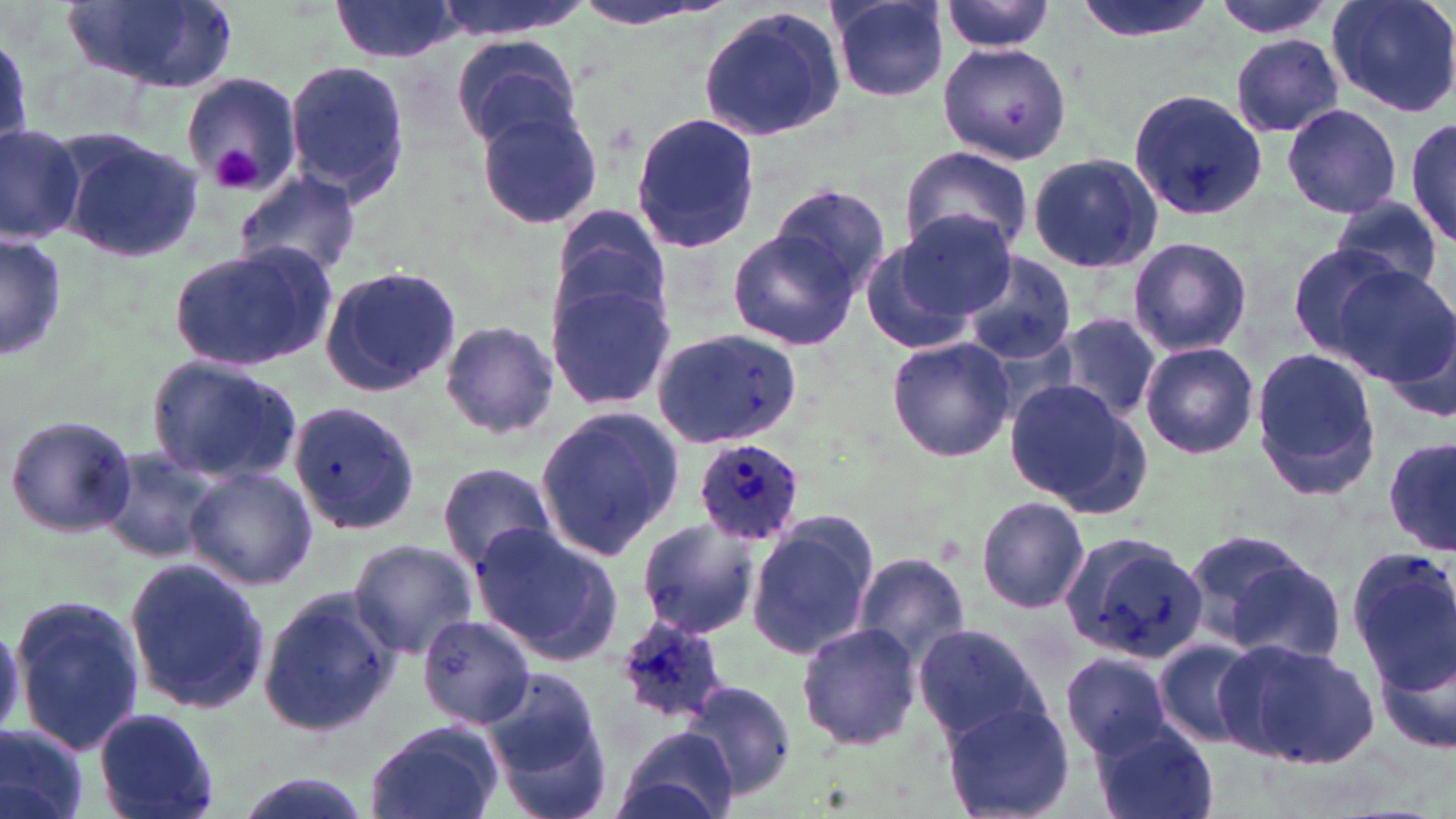 Approximate bounding boxes as named x1/y1/x2/y2 corners in pixels. Uninfected red blood cell locations: (x1=67, y1=0, x2=239, y2=93), (x1=329, y1=0, x2=463, y2=63), (x1=430, y1=0, x2=592, y2=39), (x1=570, y1=0, x2=725, y2=34), (x1=1072, y1=0, x2=1215, y2=43), (x1=1209, y1=0, x2=1343, y2=38), (x1=1325, y1=0, x2=1456, y2=118), (x1=941, y1=1, x2=1057, y2=53), (x1=829, y1=2, x2=952, y2=102), (x1=699, y1=5, x2=849, y2=141), (x1=453, y1=33, x2=582, y2=150), (x1=1230, y1=35, x2=1345, y2=137), (x1=938, y1=41, x2=1072, y2=166), (x1=286, y1=59, x2=411, y2=205), (x1=180, y1=69, x2=305, y2=195), (x1=1125, y1=90, x2=1267, y2=223), (x1=1281, y1=102, x2=1403, y2=220), (x1=474, y1=104, x2=604, y2=232), (x1=630, y1=114, x2=762, y2=254), (x1=1407, y1=116, x2=1456, y2=247), (x1=0, y1=122, x2=84, y2=243), (x1=57, y1=129, x2=203, y2=264), (x1=901, y1=145, x2=1033, y2=263), (x1=1027, y1=153, x2=1162, y2=274), (x1=232, y1=168, x2=363, y2=280), (x1=768, y1=182, x2=892, y2=298), (x1=1331, y1=198, x2=1446, y2=295), (x1=549, y1=204, x2=671, y2=338), (x1=883, y1=212, x2=1019, y2=330), (x1=728, y1=228, x2=861, y2=349), (x1=1, y1=232, x2=68, y2=363), (x1=858, y1=235, x2=985, y2=358), (x1=1128, y1=236, x2=1252, y2=356), (x1=1284, y1=244, x2=1404, y2=356), (x1=168, y1=245, x2=333, y2=373), (x1=961, y1=251, x2=1081, y2=363), (x1=318, y1=265, x2=462, y2=397), (x1=1329, y1=267, x2=1456, y2=389), (x1=544, y1=278, x2=678, y2=414), (x1=1055, y1=313, x2=1162, y2=423), (x1=439, y1=321, x2=558, y2=439), (x1=656, y1=327, x2=803, y2=450), (x1=887, y1=336, x2=1015, y2=462), (x1=1140, y1=340, x2=1260, y2=460), (x1=1249, y1=346, x2=1385, y2=500), (x1=145, y1=355, x2=302, y2=488), (x1=1004, y1=378, x2=1145, y2=511), (x1=288, y1=400, x2=420, y2=536), (x1=534, y1=405, x2=684, y2=562), (x1=3, y1=414, x2=138, y2=538), (x1=1385, y1=436, x2=1456, y2=558), (x1=98, y1=446, x2=225, y2=565), (x1=436, y1=463, x2=558, y2=571), (x1=183, y1=465, x2=318, y2=590), (x1=976, y1=497, x2=1090, y2=613), (x1=746, y1=515, x2=879, y2=661), (x1=634, y1=517, x2=763, y2=641), (x1=470, y1=523, x2=624, y2=666), (x1=1060, y1=527, x2=1208, y2=682), (x1=1180, y1=527, x2=1318, y2=645), (x1=348, y1=539, x2=481, y2=657), (x1=1350, y1=546, x2=1456, y2=693), (x1=853, y1=552, x2=972, y2=667), (x1=1220, y1=555, x2=1346, y2=666), (x1=123, y1=556, x2=269, y2=718), (x1=256, y1=586, x2=400, y2=741), (x1=9, y1=594, x2=147, y2=758), (x1=413, y1=613, x2=536, y2=731), (x1=795, y1=622, x2=921, y2=752), (x1=912, y1=623, x2=1050, y2=744), (x1=1374, y1=637, x2=1456, y2=758), (x1=1155, y1=638, x2=1260, y2=748), (x1=1219, y1=638, x2=1379, y2=769), (x1=1061, y1=652, x2=1175, y2=758), (x1=486, y1=670, x2=609, y2=811), (x1=662, y1=688, x2=792, y2=812), (x1=941, y1=699, x2=1073, y2=819), (x1=94, y1=706, x2=222, y2=819), (x1=1090, y1=719, x2=1220, y2=819), (x1=0, y1=722, x2=90, y2=819), (x1=361, y1=724, x2=502, y2=819), (x1=614, y1=727, x2=738, y2=819), (x1=229, y1=772, x2=376, y2=819). Platelet locations: (x1=213, y1=146, x2=262, y2=192). Plasmodium ovale-infected red blood cell locations: (x1=695, y1=438, x2=806, y2=544), (x1=611, y1=615, x2=733, y2=729). Slide-level diagnosis: Plasmodium ovale. Thin blood film. Optical microscopy. Image is 1456×819 pixels. Captured at 1000x magnification. May-Grünwald-Giemsa-stained preparation. Single field of view.